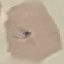

malaria status = parasitized
stain = Giemsa
capture = smartphone through the microscope eyepiece
preparation = thin smear
image type = cell patch, automatically extracted from a larger field of view and resized to 64 × 64 pixels